Name the parasite shown.
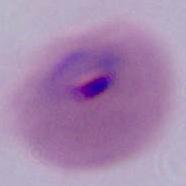

This is Plasmodium.

{
  "magnification": "400x or 1000x",
  "modality": "micrograph"
}